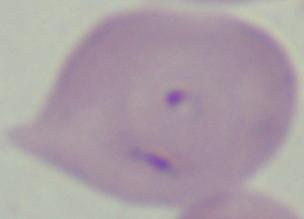 Micrograph. A Babesia parasite is seen. Captured at 1000x magnification.